Give the position of every Plasmodium parasite visible.
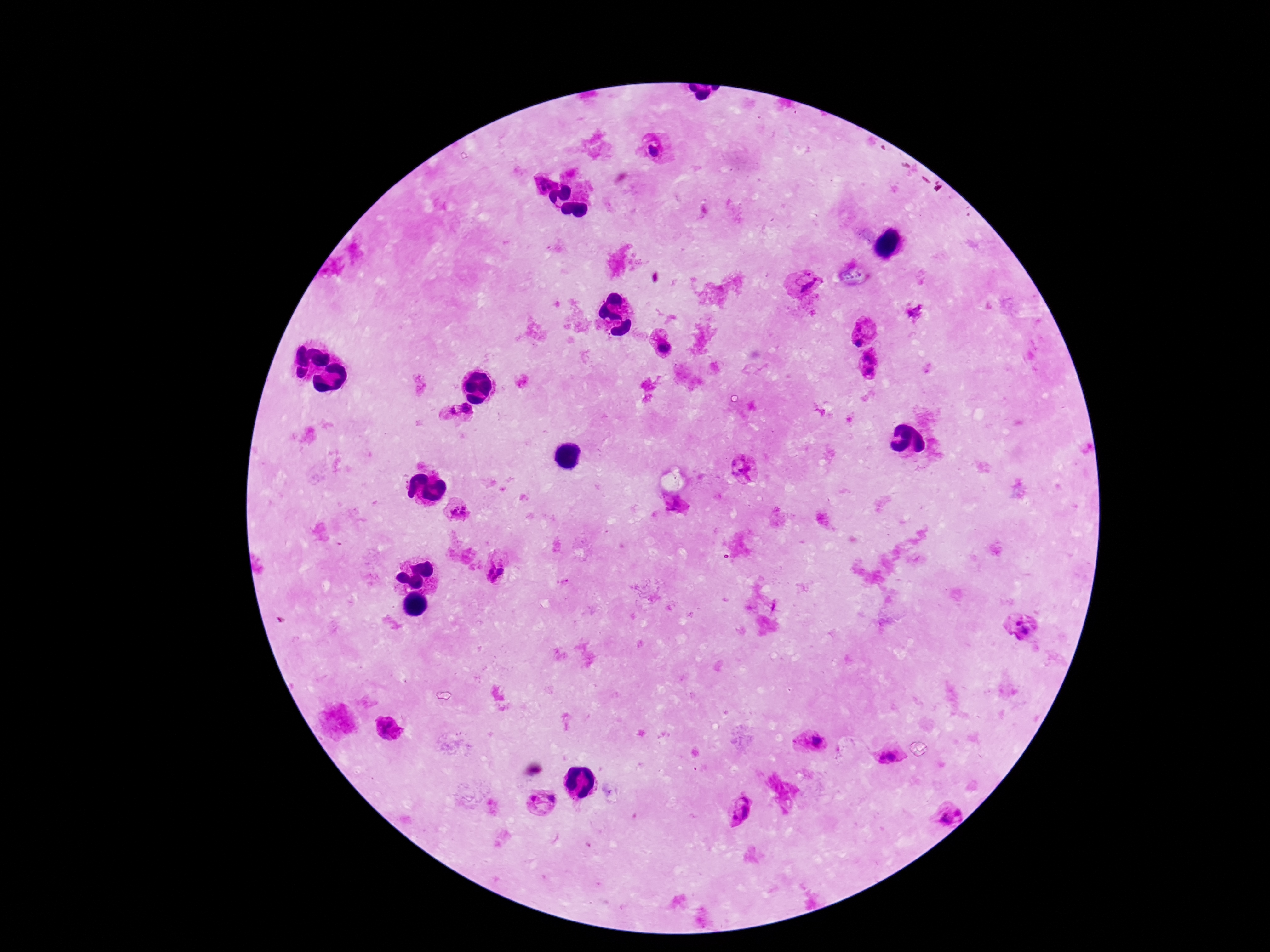
Approximate centers as [x, y] in pixels.
Plasmodium parasites: [656, 151], [544, 184], [805, 285], [864, 330], [663, 345], [868, 364], [466, 409], [449, 411], [743, 469], [676, 503], [459, 511], [495, 571], [1023, 627], [389, 729], [815, 742], [889, 756], [542, 802], [740, 810], [950, 814].

field_of_view: one from this slide
image_size: 1270×952 pixels
stain: Giemsa
magnification: 100x
patient_malaria_status: positive
preparation: thick peripheral-blood smear
capture: smartphone camera through the microscope eyepiece